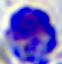

Summary:
  - Magnification: 400x
  - Identification: leukocyte
  - Modality: photomicrograph